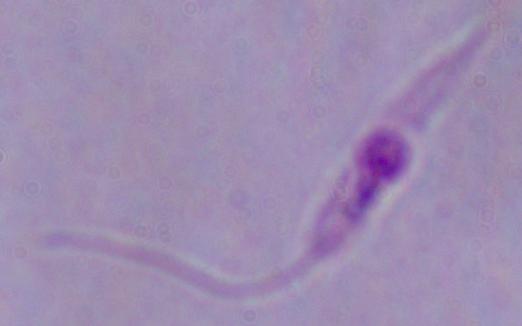

magnification = 1000x
identification = Leishmania
modality = micrograph